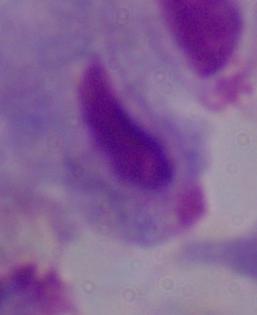

Summary:
  - Magnification: 1000x
  - Identification: trichomonad
  - Modality: photomicrograph